Report the malaria status of this cell.
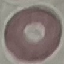
It is uninfected.

Summary:
  - Preparation: thin blood smear
  - Image type: automatically extracted cell patch, resized to 64 × 64 pixels
  - Capture: smartphone camera at the microscope eyepiece
  - Stain: Giemsa